Locate every blood parasite and identify its species.
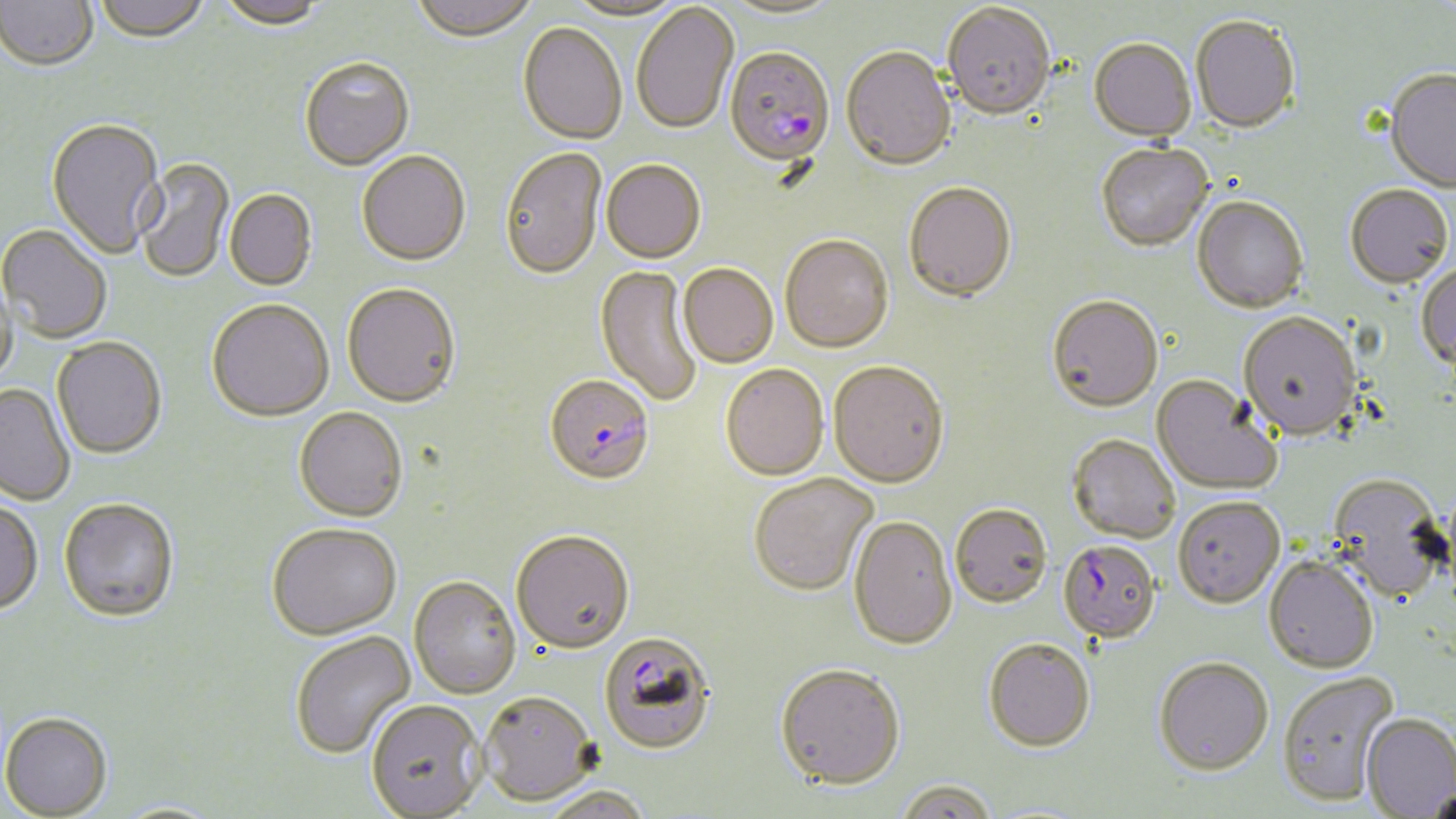

Approximate bounding boxes as [x1, y1, x2, y2] in pixels.
Plasmodium falciparum-infected red blood cells: [724, 47, 835, 168], [545, 374, 655, 485], [1063, 541, 1158, 644], [599, 631, 717, 754].
No Plasmodium ovale, Plasmodium malariae, Plasmodium vivax, Babesia divergens, or Trypanosoma brucei observed.

Uninfected red blood cell locations: [0, 0, 98, 72], [92, 0, 210, 45], [215, 0, 327, 31], [408, 0, 540, 41], [564, 0, 689, 21], [719, 1, 845, 21], [631, 2, 740, 135], [942, 5, 1056, 123], [1190, 18, 1300, 135], [518, 22, 627, 144], [1088, 40, 1197, 144], [841, 48, 956, 173], [299, 57, 414, 171], [1384, 71, 1456, 194], [45, 118, 166, 261], [1096, 145, 1214, 254], [499, 146, 607, 281], [356, 151, 471, 266], [135, 158, 235, 284], [601, 159, 706, 263], [903, 183, 1017, 304], [1345, 186, 1453, 291], [225, 190, 317, 291], [1192, 198, 1308, 315], [0, 225, 112, 344], [779, 234, 894, 354], [678, 263, 778, 368], [595, 265, 703, 408], [1415, 265, 1456, 373], [1, 270, 19, 390], [342, 284, 461, 409], [1046, 297, 1163, 413], [207, 300, 334, 423], [1238, 314, 1362, 442], [51, 337, 167, 461], [828, 361, 949, 488], [720, 364, 828, 481], [1152, 376, 1282, 497], [0, 383, 75, 507], [294, 407, 408, 523], [1068, 434, 1181, 543], [749, 472, 878, 596], [1325, 475, 1451, 605], [1172, 496, 1284, 609], [59, 498, 179, 623], [0, 500, 43, 616], [950, 504, 1052, 609], [849, 516, 957, 650], [266, 523, 402, 640], [511, 529, 635, 653], [1264, 555, 1379, 674], [408, 575, 521, 699], [290, 630, 415, 759], [984, 639, 1095, 755], [1153, 659, 1274, 777], [774, 663, 905, 792], [1277, 671, 1400, 807], [480, 690, 598, 805], [366, 699, 487, 818], [1, 713, 113, 818], [1361, 714, 1456, 816], [894, 781, 998, 819], [540, 785, 651, 819], [1425, 787, 1455, 819]. Slide-level diagnosis: Plasmodium falciparum. Captured at 1000x magnification. Thin blood smear. Optical microscopy. Image is 1456×819 pixels. One field of a larger specimen. May-Grünwald-Giemsa-stained preparation.